Report the malaria status of this cell.
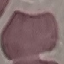

Uninfected.

image type = cell patch, automatically extracted from a larger field of view and resized to 64 × 64 pixels
preparation = thin blood film
stain = Giemsa
capture = smartphone camera at the microscope eyepiece